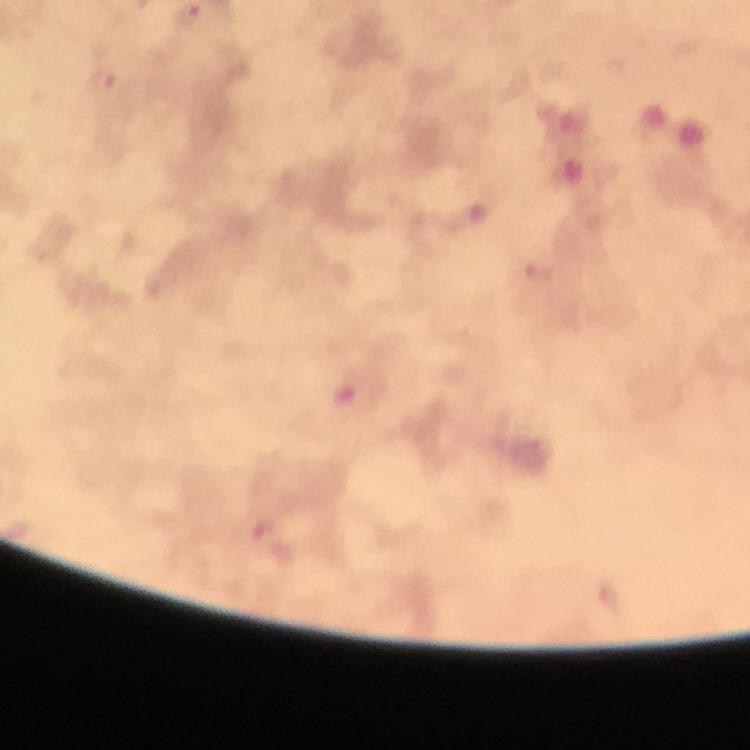
Approximate object centers, in pixels from the top-left corner.
Summary:
  - Plasmodium parasite locations: (x=187, y=16), (x=103, y=81)
  - Magnification: 100x
  - Stain: Giemsa
  - Image size: 750×750 pixels
  - Preparation: thick blood smear
  - Cropped from: one field of view
  - Immersion oil: applied
  - Context: from a malaria diagnostic workup
  - Capture: smartphone camera through the microscope